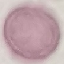

Summary:
  - Malaria status: uninfected
  - Preparation: thin blood film
  - Capture: smartphone through the microscope eyepiece
  - Image type: automatically extracted cell patch, resized to 64 × 64 pixels
  - Stain: Giemsa